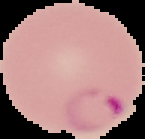

{
  "malaria_status": "parasitized",
  "image_type": "segmented cell region with the area outside set to black",
  "preparation": "thin blood smear",
  "image_size": "145×139 pixels"
}